Assess this cell for malaria.
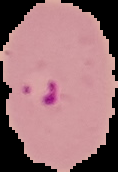
It is parasitized.

Image is 118×172 pixels. From a thin blood film. The area outside the segmented cell region is set to black.